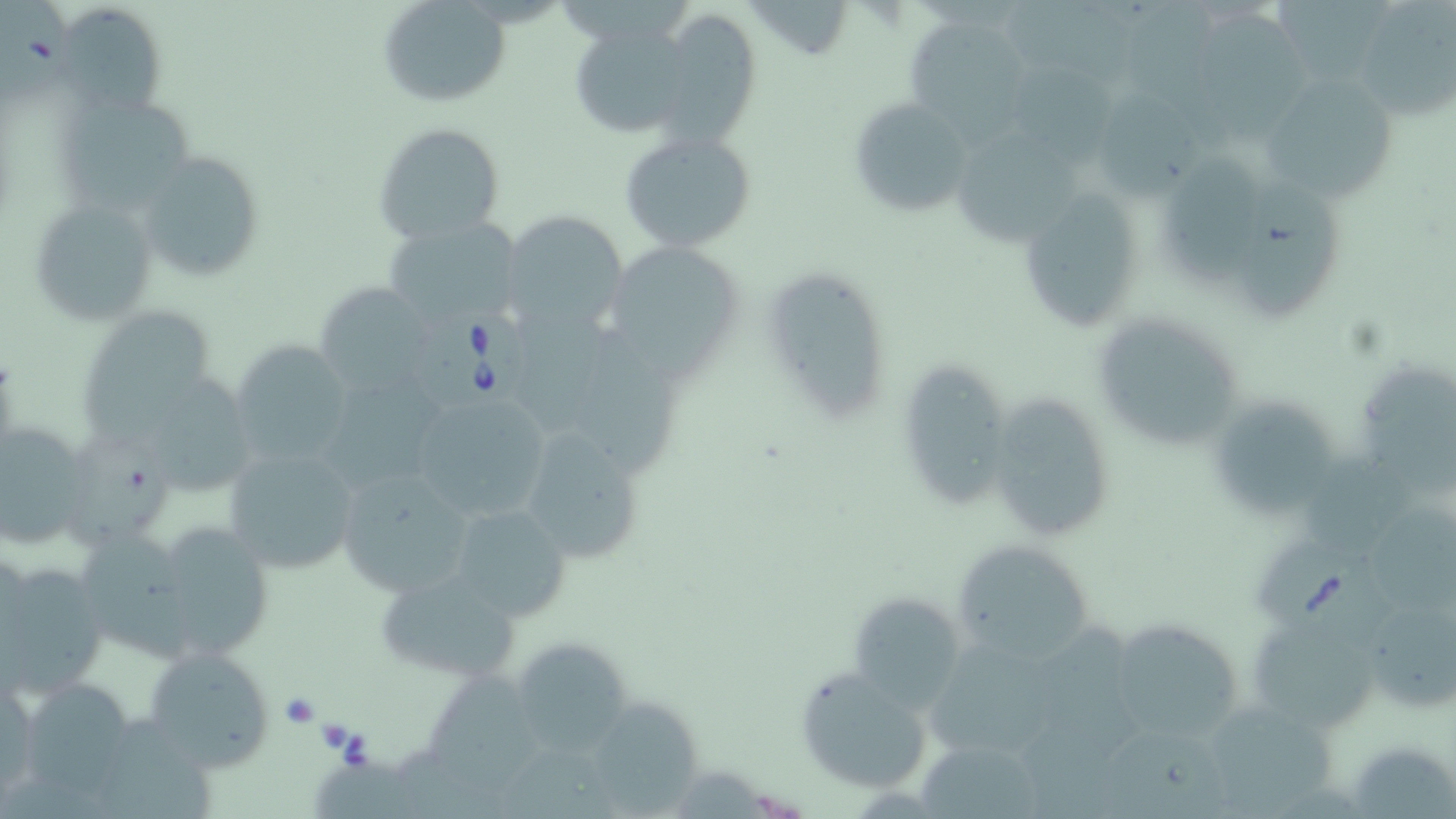

slide-level diagnosis = Babesia divergens
image size = 1456×819 pixels
field of view = single
uninfected red blood cell locations = approximate bounding boxes as (x1, y1, x2, y2) in pixels: (0, 0, 89, 112), (377, 1, 509, 108), (58, 2, 169, 113), (1118, 2, 1221, 110), (1276, 2, 1392, 83), (1003, 3, 1134, 89), (1352, 5, 1456, 121), (651, 13, 765, 146), (900, 15, 1033, 130), (1199, 19, 1312, 144), (567, 20, 694, 141), (1019, 65, 1121, 164), (1258, 74, 1400, 201), (53, 94, 198, 213), (1098, 94, 1202, 196), (847, 96, 976, 219), (372, 122, 507, 246), (618, 128, 759, 254), (960, 138, 1075, 245), (136, 149, 268, 280), (1167, 153, 1271, 282), (1245, 181, 1343, 316), (1016, 190, 1145, 334), (28, 196, 161, 326), (502, 209, 629, 341), (379, 218, 525, 336), (606, 243, 742, 387), (760, 265, 892, 425), (313, 282, 441, 398), (80, 304, 220, 425), (512, 307, 615, 439), (1091, 312, 1249, 453), (575, 334, 690, 478), (230, 339, 355, 467), (894, 359, 1015, 511), (1361, 366, 1456, 494), (328, 369, 453, 493), (131, 370, 262, 501), (407, 389, 553, 524), (985, 391, 1115, 544), (1218, 403, 1329, 517), (0, 419, 92, 551), (508, 421, 650, 564), (61, 432, 178, 552), (222, 444, 362, 576), (1299, 454, 1407, 560), (336, 467, 478, 596), (449, 503, 572, 622), (1367, 512, 1456, 616), (145, 520, 273, 660), (74, 522, 198, 674), (952, 539, 1099, 662), (0, 559, 108, 699), (372, 566, 524, 682), (845, 591, 963, 708), (1373, 606, 1456, 706), (1106, 615, 1248, 743), (1247, 615, 1384, 733), (1037, 622, 1143, 758), (923, 630, 1071, 766), (508, 637, 638, 757), (140, 643, 276, 771), (796, 666, 930, 794), (427, 670, 552, 797), (1, 676, 41, 804), (16, 677, 139, 804), (1198, 699, 1339, 818), (597, 700, 695, 812), (96, 714, 213, 818), (1105, 727, 1227, 819), (920, 744, 1039, 819), (1351, 748, 1456, 819), (313, 757, 421, 818)
stain = May-Grünwald-Giemsa
magnification = 1000x
preparation = thin blood film
modality = light microscopy
Babesia divergens-infected red blood cell locations = approximate bounding boxes as (x1, y1, x2, y2) in pixels: (408, 300, 542, 413), (1248, 522, 1396, 649)